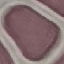
Malaria status: uninfected. Automatically extracted cell patch, resized to 64 × 64 pixels. Thin smear of blood. Photographed with a smartphone camera at the microscope eyepiece. Giemsa stain.